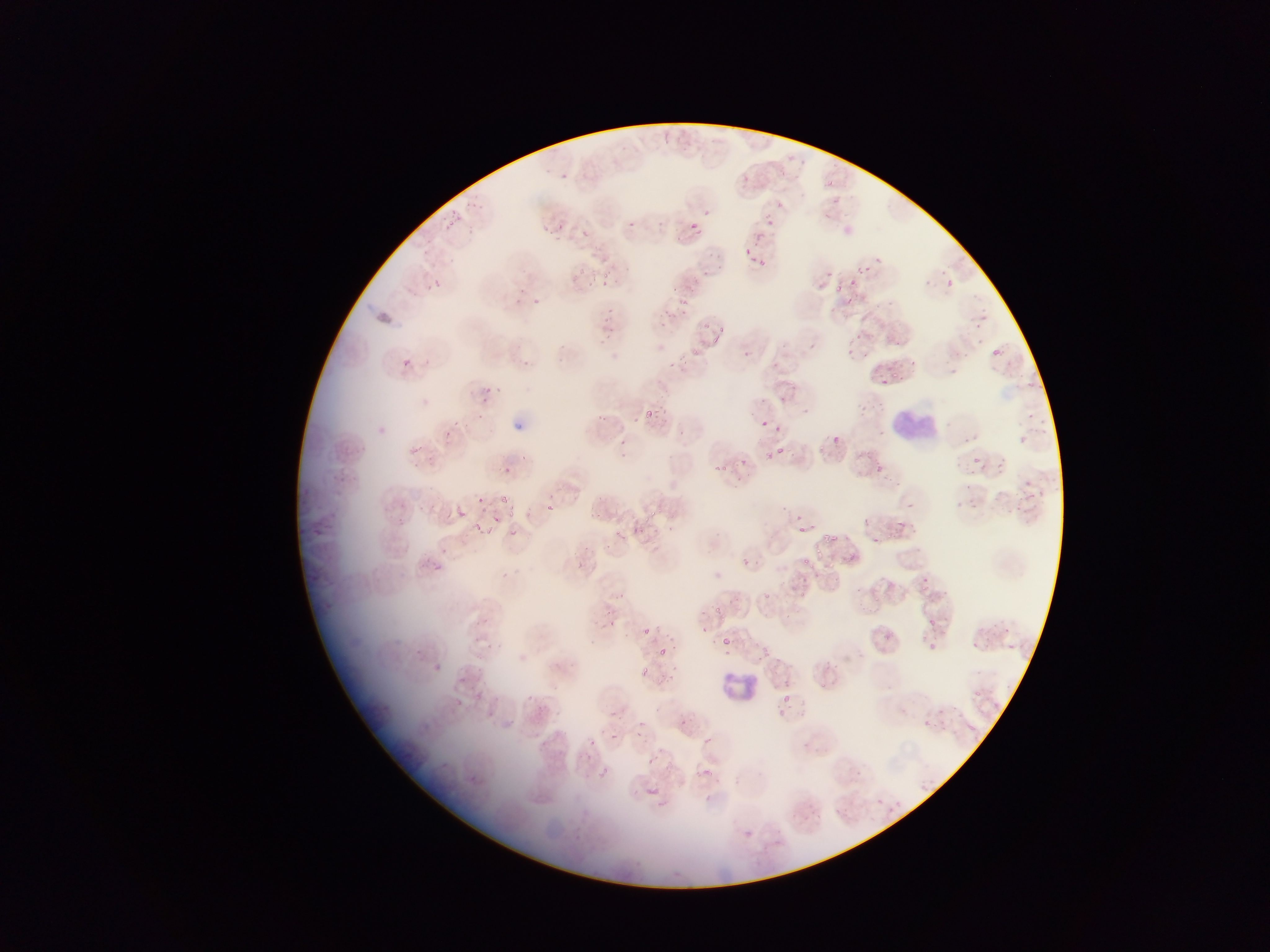
{
  "plasmodium_parasite_locations": "approximate bounding boxes as [left, top, right, bottom] in pixels: [742, 175, 750, 182], [826, 180, 836, 190], [831, 200, 839, 206], [777, 201, 783, 209], [449, 210, 460, 217], [702, 210, 710, 215], [762, 214, 774, 227], [447, 219, 454, 227], [687, 219, 703, 234], [626, 221, 637, 230], [542, 225, 552, 237], [580, 229, 591, 239], [754, 231, 764, 241], [745, 247, 753, 256], [751, 255, 759, 265], [875, 255, 882, 263], [758, 260, 768, 268], [856, 264, 865, 275], [578, 267, 587, 276], [940, 269, 945, 280], [827, 270, 833, 279], [603, 272, 612, 279], [850, 277, 860, 287], [430, 278, 444, 291], [946, 279, 955, 289], [925, 280, 935, 290], [599, 281, 607, 288], [517, 287, 526, 293], [844, 296, 857, 307], [513, 297, 523, 307], [533, 298, 541, 303], [888, 298, 896, 306], [677, 299, 686, 307], [979, 314, 993, 323], [603, 315, 613, 328], [703, 320, 711, 327], [720, 323, 726, 332], [604, 332, 617, 342], [708, 335, 720, 342], [978, 337, 985, 345], [559, 342, 567, 352], [992, 347, 1007, 358], [693, 349, 699, 357], [845, 349, 854, 356], [402, 357, 412, 367], [521, 359, 533, 368], [910, 359, 918, 368], [940, 359, 948, 365], [950, 367, 959, 374], [494, 383, 502, 391], [483, 385, 496, 400], [644, 409, 653, 417], [652, 410, 658, 421], [477, 414, 488, 424], [600, 414, 607, 422], [634, 416, 639, 424], [1041, 418, 1048, 426], [762, 419, 771, 429], [943, 420, 951, 429], [1019, 436, 1031, 448], [418, 440, 425, 452], [779, 447, 786, 455], [619, 448, 628, 458], [764, 451, 778, 464], [519, 454, 530, 461], [974, 457, 980, 465], [711, 462, 722, 472], [997, 462, 1004, 472], [720, 463, 728, 470], [876, 463, 885, 472], [956, 463, 964, 471], [968, 469, 979, 475], [966, 484, 977, 492], [500, 493, 509, 501], [550, 494, 557, 502], [1028, 494, 1036, 501], [476, 497, 486, 505], [971, 498, 976, 508], [953, 501, 963, 508], [546, 502, 556, 511], [907, 503, 916, 513], [456, 505, 465, 514], [592, 505, 601, 518], [506, 510, 519, 519], [491, 515, 500, 523], [620, 516, 630, 522], [642, 516, 651, 521], [862, 517, 869, 526], [897, 519, 905, 526], [473, 521, 484, 530], [668, 524, 675, 533], [612, 525, 621, 537], [485, 526, 493, 532], [632, 527, 641, 533], [822, 531, 834, 540], [606, 542, 612, 552], [813, 543, 823, 557], [583, 544, 593, 556], [441, 547, 449, 556], [745, 558, 750, 566], [573, 561, 584, 569], [619, 592, 626, 601], [765, 592, 772, 604], [715, 604, 723, 614], [483, 616, 489, 624], [928, 619, 936, 627], [610, 620, 618, 627], [642, 627, 650, 635], [701, 627, 709, 632], [669, 634, 675, 642], [721, 636, 732, 646], [590, 640, 598, 648], [485, 642, 494, 652], [656, 648, 669, 657], [724, 650, 734, 656], [758, 654, 762, 662], [434, 664, 441, 672], [641, 666, 651, 677], [477, 667, 486, 676], [665, 673, 676, 682], [526, 693, 536, 702], [784, 694, 791, 703], [640, 719, 646, 727], [610, 731, 619, 740], [637, 731, 647, 741], [588, 736, 597, 746], [702, 737, 711, 745], [645, 756, 657, 766], [602, 767, 608, 777], [706, 793, 714, 806] | approximate [x, y] pixel centers of objects too small to bound: [564, 177], [659, 224], [561, 227], [869, 266], [706, 273], [838, 286], [674, 289], [978, 327], [859, 336], [864, 353], [957, 354], [967, 355], [562, 358], [901, 364], [896, 375], [883, 381], [1031, 384], [783, 398], [762, 400], [661, 406], [1033, 417], [454, 424], [466, 424], [780, 427], [445, 432], [683, 432], [837, 440], [966, 440], [621, 441], [431, 459], [743, 459], [506, 470], [1028, 482], [994, 498], [1016, 504], [654, 512], [800, 516], [640, 528], [801, 529], [514, 530], [875, 540], [430, 560], [807, 561], [610, 614], [715, 640], [674, 647], [763, 648], [573, 665], [676, 668], [825, 685], [781, 711], [683, 722], [706, 771]",
  "leukocyte_locations": "approximate bounding boxes as [left, top, right, bottom] in pixels: [892, 399, 929, 446], [718, 668, 758, 708]",
  "preparation": "thin blood film",
  "capture": "mobile-phone photograph through a microscope",
  "field_of_view": "single",
  "image_size": "1270×952 pixels",
  "country": "Ghana"
}